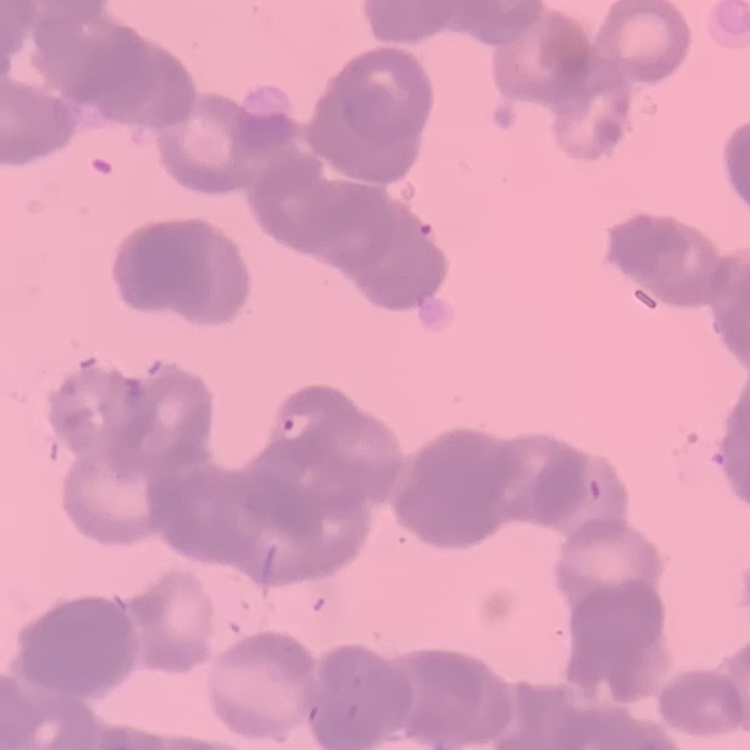 The erythrocytes exhibit rouleaux formation. Stained with either Field's or Giemsa. Square crop of a larger photomicrograph. Thin peripheral smear.